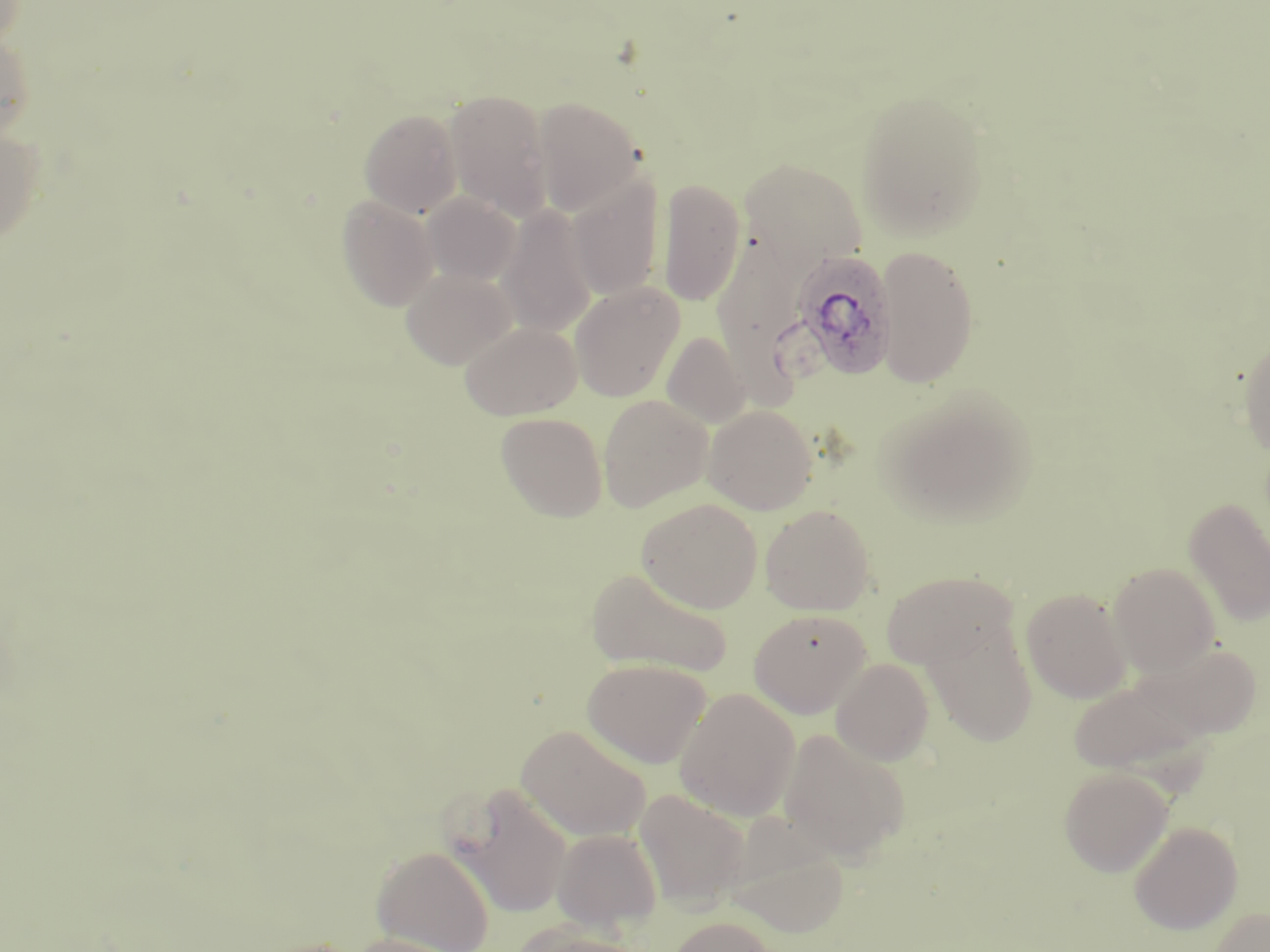

Summary:
  - Coordinate format: approximate bounding boxes as (x1, y1, x2, y2) in pixels
  - Uninfected red blood cell locations: (0, 33, 35, 141), (444, 89, 554, 221), (855, 89, 991, 242), (532, 97, 645, 216), (359, 108, 463, 218), (0, 126, 46, 245), (739, 157, 869, 272), (567, 174, 665, 300), (658, 178, 746, 306), (422, 192, 521, 286), (336, 195, 440, 312), (496, 205, 598, 336), (713, 225, 812, 391), (875, 245, 980, 387), (401, 268, 517, 369), (569, 282, 685, 402), (460, 321, 581, 420), (662, 332, 750, 429), (1238, 335, 1270, 458), (883, 389, 1037, 526), (597, 395, 713, 512), (703, 404, 818, 515), (496, 412, 608, 522), (1183, 497, 1270, 627), (637, 499, 762, 613), (760, 505, 876, 615), (1108, 562, 1220, 678), (586, 566, 732, 679), (879, 569, 1018, 671), (1125, 584, 1238, 733), (1021, 587, 1133, 704), (749, 609, 872, 717), (922, 616, 1038, 747), (1141, 642, 1263, 740), (582, 658, 712, 768), (831, 658, 935, 766), (1069, 674, 1209, 778), (674, 688, 801, 821), (516, 724, 652, 842), (778, 728, 909, 863), (1059, 767, 1173, 877), (449, 781, 573, 919), (634, 789, 750, 910), (722, 819, 849, 938), (1128, 821, 1243, 934), (551, 828, 663, 931), (372, 845, 494, 952), (1208, 907, 1270, 952), (668, 916, 777, 952), (510, 920, 644, 952), (346, 933, 467, 952)
  - Plasmodium ovale-infected red blood cell locations: (792, 249, 897, 382)
  - Slide-level diagnosis: Plasmodium ovale
  - Field of view: one of a larger specimen
  - Modality: optical microscopy
  - Magnification: 1000x
  - Preparation: thin blood film
  - Image size: 1270×952 pixels
  - Stain: May-Grünwald-Giemsa